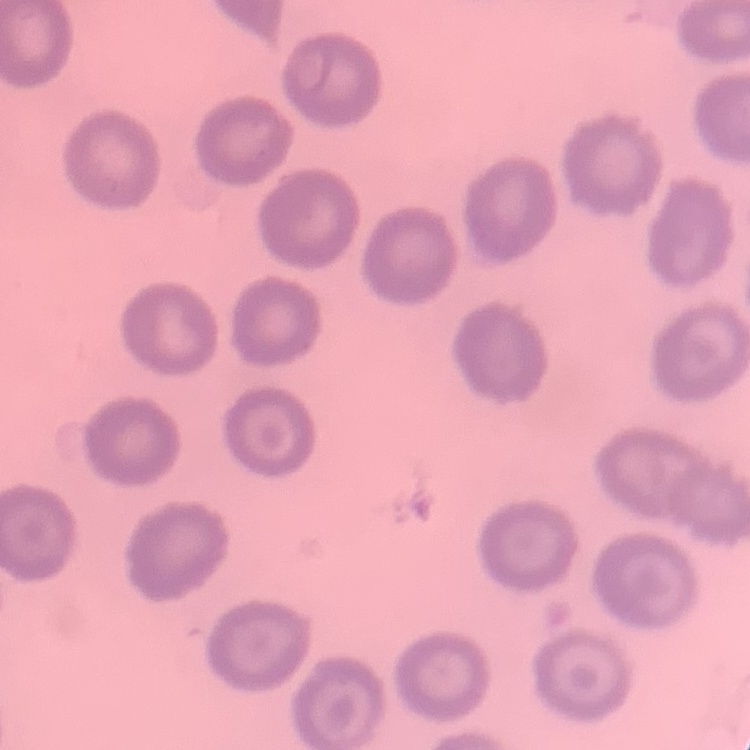
The erythrocytes show no rouleaux formation. One tile cut from a larger photomicrograph. Thin peripheral smear. Field's or Giemsa stain.